Name the cell type shown.
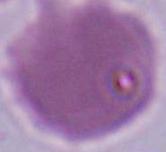
An erythrocyte.

Summary:
  - Modality: micrograph
  - Magnification: 1000x